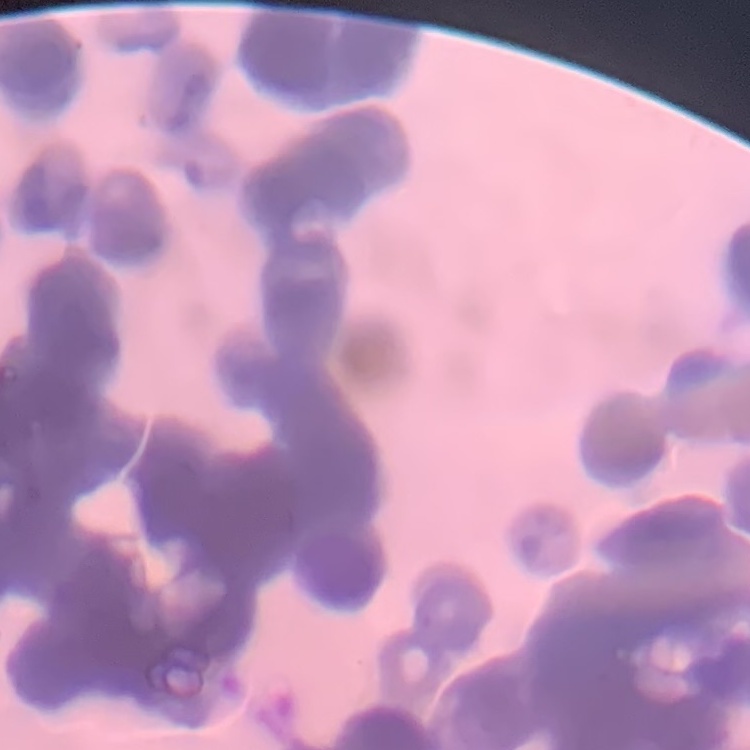

Summary:
  - Red blood cell morphology: rouleaux formation
  - Preparation: thin peripheral smear
  - Image type: one tile cut from a larger photomicrograph
  - Stain: Field's or Giemsa